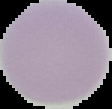

preparation: thin blood smear
image_type: cell region segmented out of the field of view; surrounding area masked to black
result: no malaria parasites detected
image_size: 112×109 pixels